Name the parasite shown.
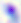
This is Toxoplasma gondii.

magnification = 400x
modality = photomicrograph